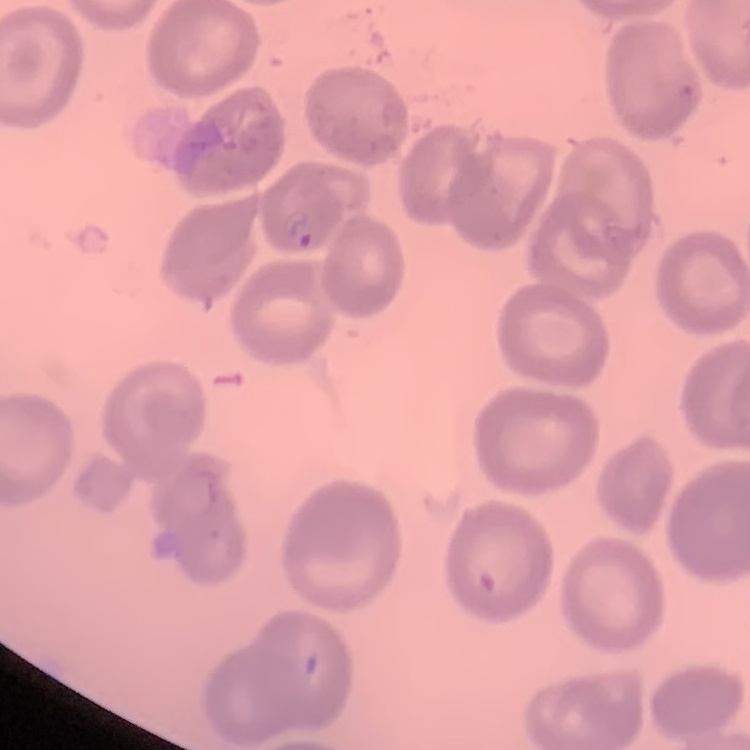

{
  "red_blood_cell_morphology": "no rouleaux formation",
  "image_type": "square crop of a larger photomicrograph",
  "preparation": "thin blood film",
  "stain": "Field's or Giemsa"
}